Name the parasite shown.
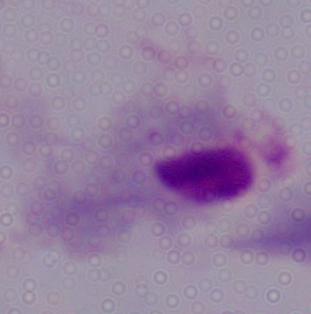

This is a trichomonad.

modality = micrograph
magnification = 1000x